Comment on the morphology of the red blood cells.
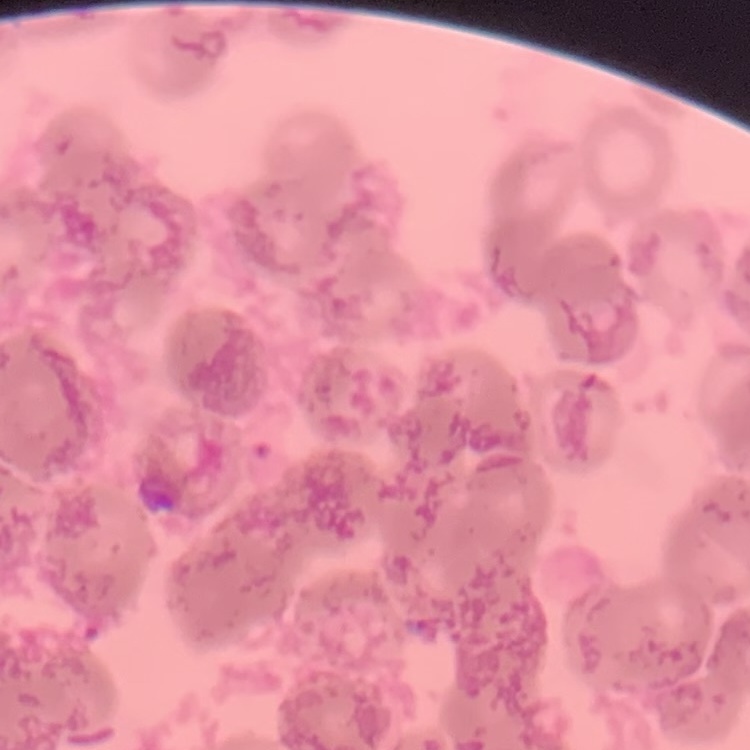

Rouleaux formation.

Square crop of a larger photomicrograph. Field's or Giemsa stain. Thin peripheral smear.